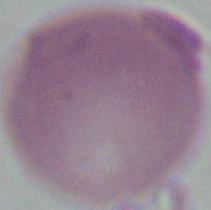

Photomicrograph. A red blood cell is seen. Captured at 1000x magnification.